Report the malaria status of this cell.
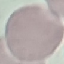
It is uninfected.

Summary:
  - Stain: Giemsa
  - Image type: automatically extracted cell patch, resized to 64 × 64 pixels
  - Capture: smartphone camera at the microscope eyepiece
  - Preparation: thin smear